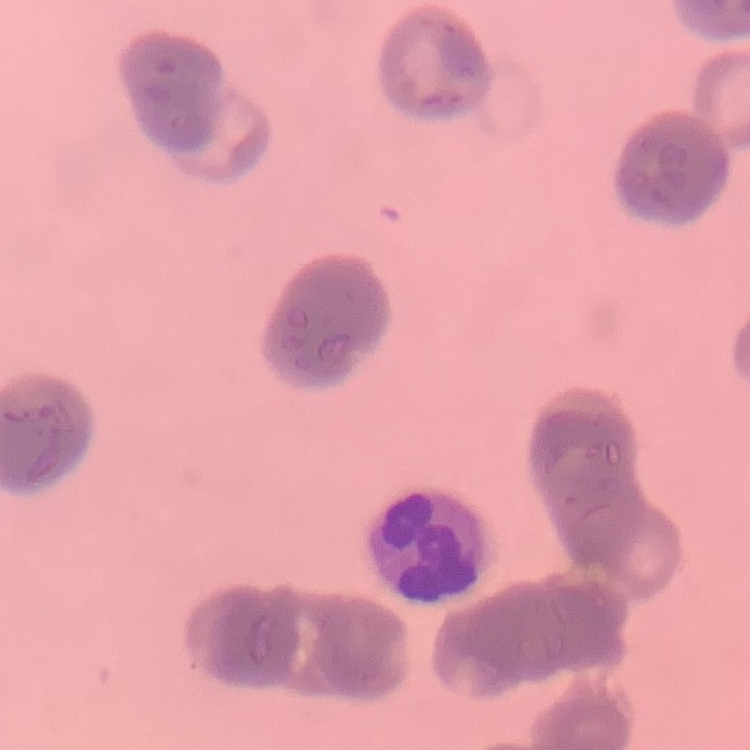

erythrocyte morphology = rouleaux formation
image type = one tile cut from a larger photomicrograph
preparation = thin blood smear
stain = Field's or Giemsa